Comment on the morphology of the red blood cells.
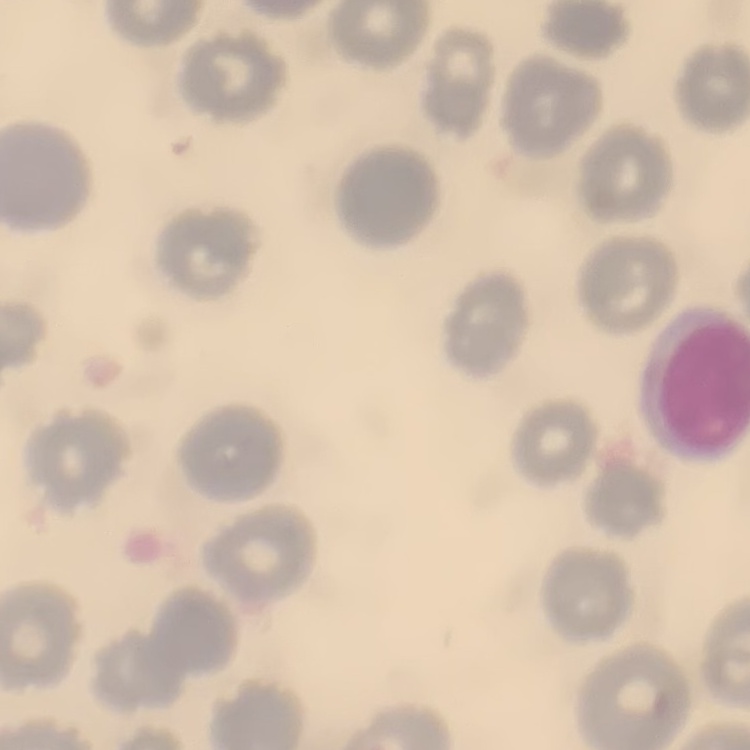

No rouleaux formation.

stain = Field's or Giemsa
image type = square crop of a larger photomicrograph
preparation = thin peripheral smear